Assess this cell for malaria.
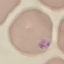

Parasitized.

Summary:
  - Preparation: thin blood film
  - Stain: Giemsa
  - Capture: smartphone through the microscope eyepiece
  - Image type: cell patch, automatically extracted from a larger field of view and resized to 64 × 64 pixels